State which parasite is depicted.
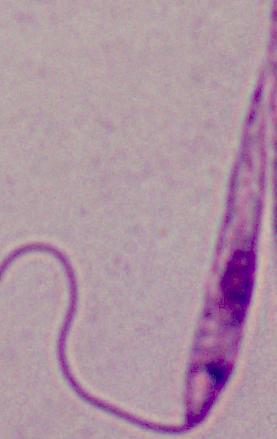
Leishmania.

Summary:
  - Magnification: 1000x
  - Modality: micrograph